Classify this cell by malaria status.
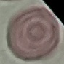
It is uninfected.

Giemsa-stained preparation. Thin blood film. Acquired by smartphone through the microscope eyepiece. Automatically extracted cell patch, resized to 64 × 64 pixels.